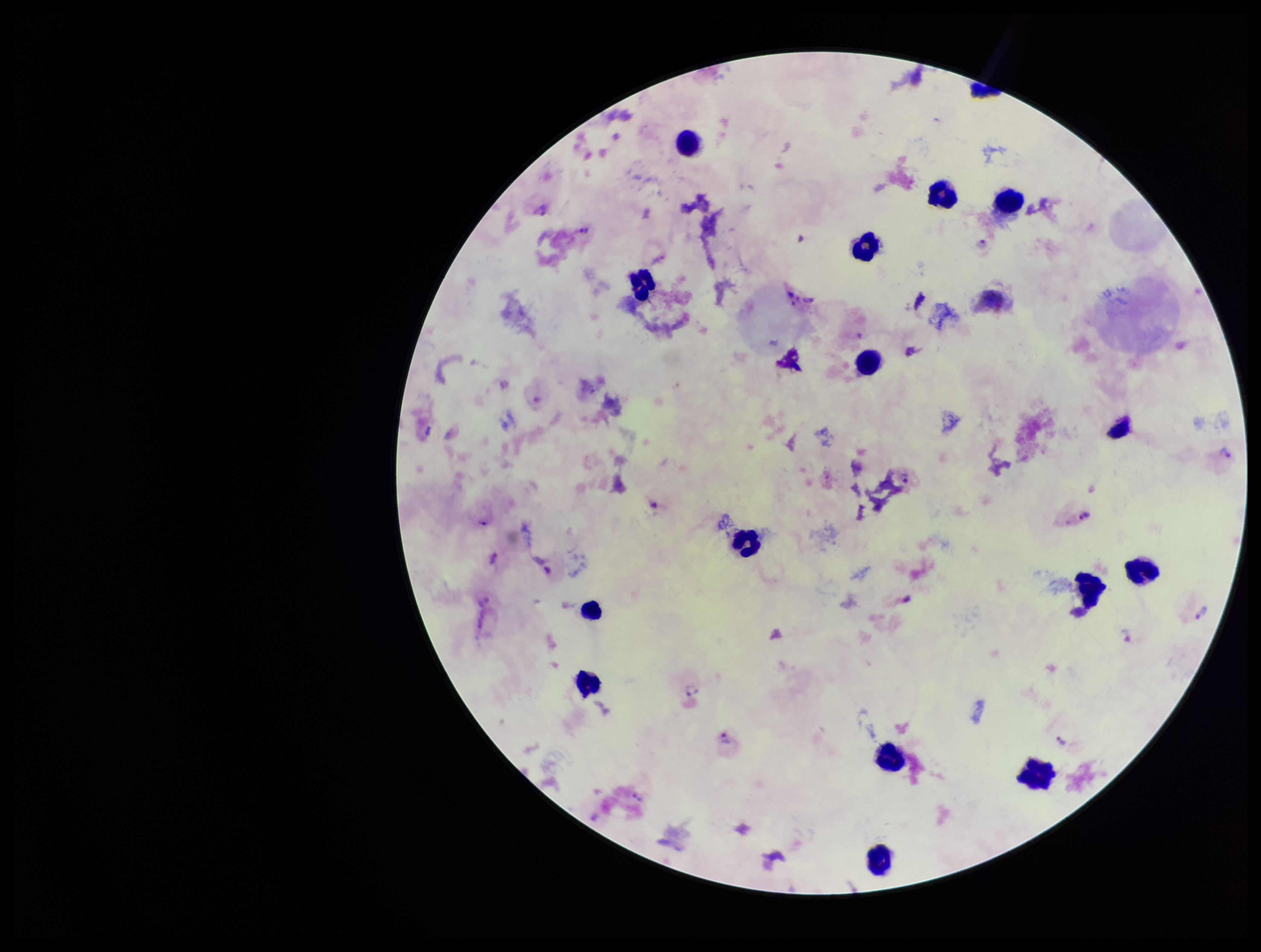

Summary:
  - Patient malaria status: positive
  - Field of view: one from this slide
  - Stain: Giemsa
  - Leukocyte count: 16
  - Preparation: thick blood smear
  - Capture: smartphone photograph through the microscope eyepiece
  - Image size: 1261×952 pixels
  - Plasmodium parasites: detected
  - Parasite count: 18
  - Species reported for this patient: Plasmodium vivax